State the blood parasite species.
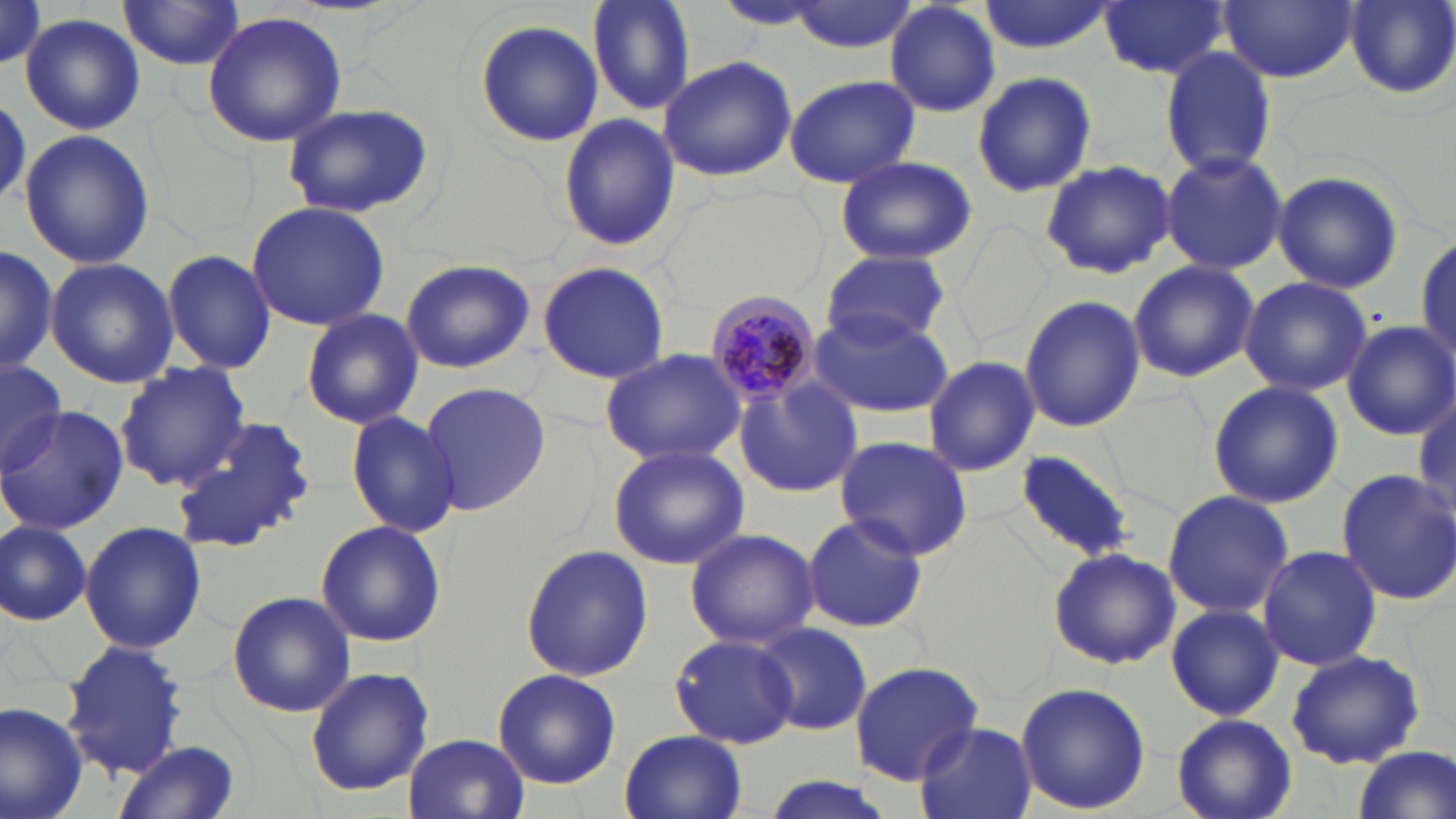
Plasmodium malariae.

Summary:
  - Coordinate format: approximate bounding boxes as (x1, y1, x2, y2) in pixels
  - Uninfected red blood cell locations: (588, 0, 696, 115), (974, 0, 1115, 54), (1098, 0, 1231, 81), (1219, 0, 1357, 83), (1345, 0, 1456, 100), (115, 1, 247, 72), (784, 1, 920, 53), (713, 2, 829, 31), (884, 2, 1001, 117), (19, 12, 146, 135), (203, 12, 346, 147), (476, 20, 604, 147), (1159, 47, 1278, 177), (656, 56, 795, 179), (971, 70, 1097, 197), (783, 75, 919, 188), (0, 95, 29, 210), (282, 100, 436, 220), (556, 113, 680, 253), (19, 130, 154, 270), (1161, 149, 1288, 277), (832, 155, 978, 266), (1040, 159, 1175, 279), (1273, 169, 1404, 295), (246, 201, 390, 330), (1415, 232, 1455, 366), (0, 245, 56, 376), (163, 248, 277, 374), (819, 250, 950, 350), (399, 257, 536, 374), (46, 258, 181, 389), (1128, 260, 1258, 382), (537, 261, 670, 385), (1238, 276, 1372, 395), (1018, 295, 1145, 433), (806, 304, 956, 418), (300, 307, 425, 430), (1340, 319, 1456, 440), (600, 349, 746, 465), (0, 356, 67, 473), (923, 356, 1041, 476), (115, 362, 252, 489), (736, 377, 863, 496), (418, 379, 552, 515), (1206, 381, 1344, 509), (0, 407, 130, 533), (345, 409, 462, 538), (171, 418, 313, 555), (834, 435, 974, 560), (608, 443, 751, 570), (1016, 448, 1134, 562), (1335, 469, 1456, 604), (1161, 489, 1292, 619), (801, 513, 926, 633), (314, 519, 447, 649), (0, 520, 91, 627), (79, 521, 206, 655), (685, 530, 817, 648), (1257, 544, 1383, 671), (521, 545, 655, 683), (1048, 548, 1179, 670), (227, 590, 355, 718), (1166, 603, 1283, 721), (755, 622, 872, 736), (669, 632, 799, 749), (62, 639, 189, 781), (1285, 650, 1425, 768), (850, 662, 983, 785), (304, 668, 436, 796), (491, 669, 621, 789), (1015, 681, 1151, 815), (0, 701, 90, 819), (1170, 714, 1298, 819), (912, 720, 1036, 819), (620, 730, 747, 819), (404, 734, 530, 819), (114, 740, 240, 819), (1345, 748, 1454, 819), (754, 776, 900, 819)
  - Plasmodium malariae-infected red blood cell locations: (704, 288, 824, 408)
  - Stain: May-Grünwald-Giemsa
  - Preparation: thin blood film
  - Image size: 1456×819 pixels
  - Field of view: one of a larger specimen
  - Modality: light microscopy
  - Magnification: 1000x